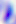
Captured at 400x magnification. Photomicrograph. Toxoplasma gondii is shown.